Locate every P. falciparum parasite and identify its life-cycle stage.
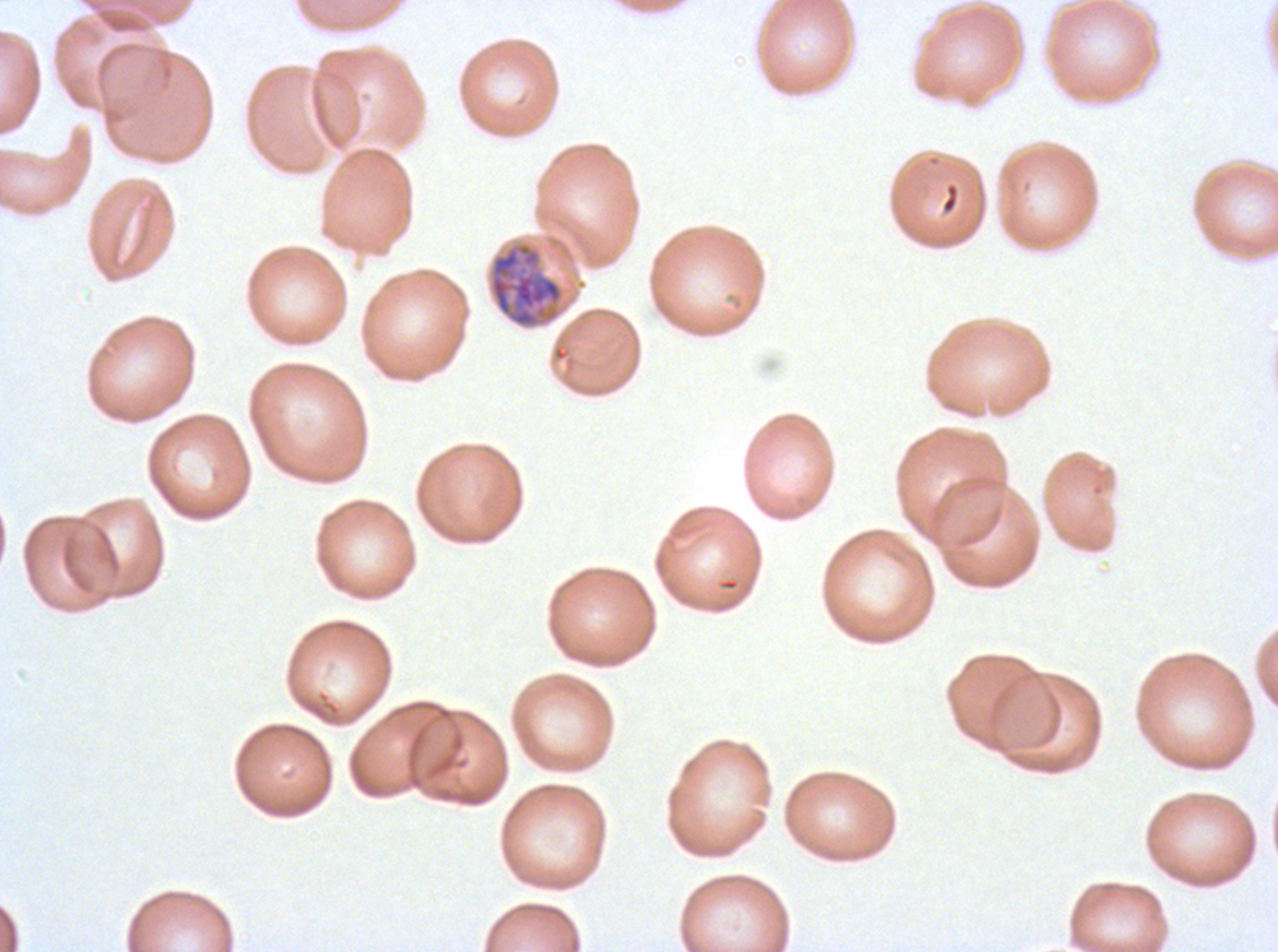
Approximate bounding boxes as {x1, y1, x2, y2} in pixels.
Mid trophozoites: {488, 242, 564, 329}.
No rings, late-ring/early-trophozoite forms, late trophozoites, early schizonts, late schizonts, segmenters, or gametocytes observed.

P. falciparum from a patient in The Gambia, cultured ex vivo for 24 to 48 hours. A sub-image separated from a larger composite. Giemsa-stained preparation. Image is 1278×952 pixels. Thin blood film.